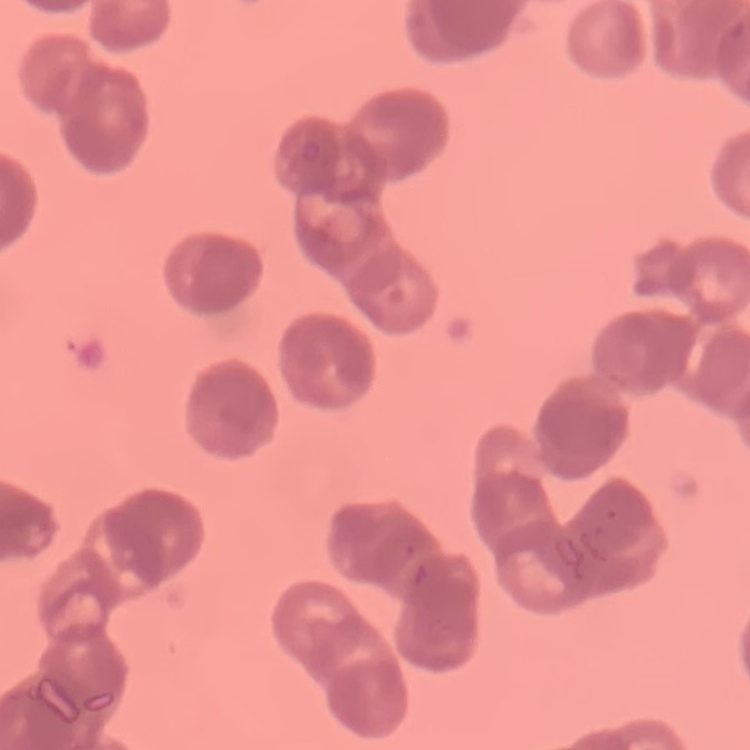
{
  "erythrocyte_morphology": "rouleaux formation",
  "image_type": "square crop of a larger photomicrograph",
  "stain": "Field's or Giemsa",
  "preparation": "thin blood smear"
}